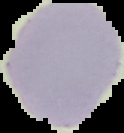

Summary:
  - Malaria status: uninfected
  - Image type: segmented cell region with the area outside set to black
  - Image size: 124×133 pixels
  - Preparation: thin blood smear